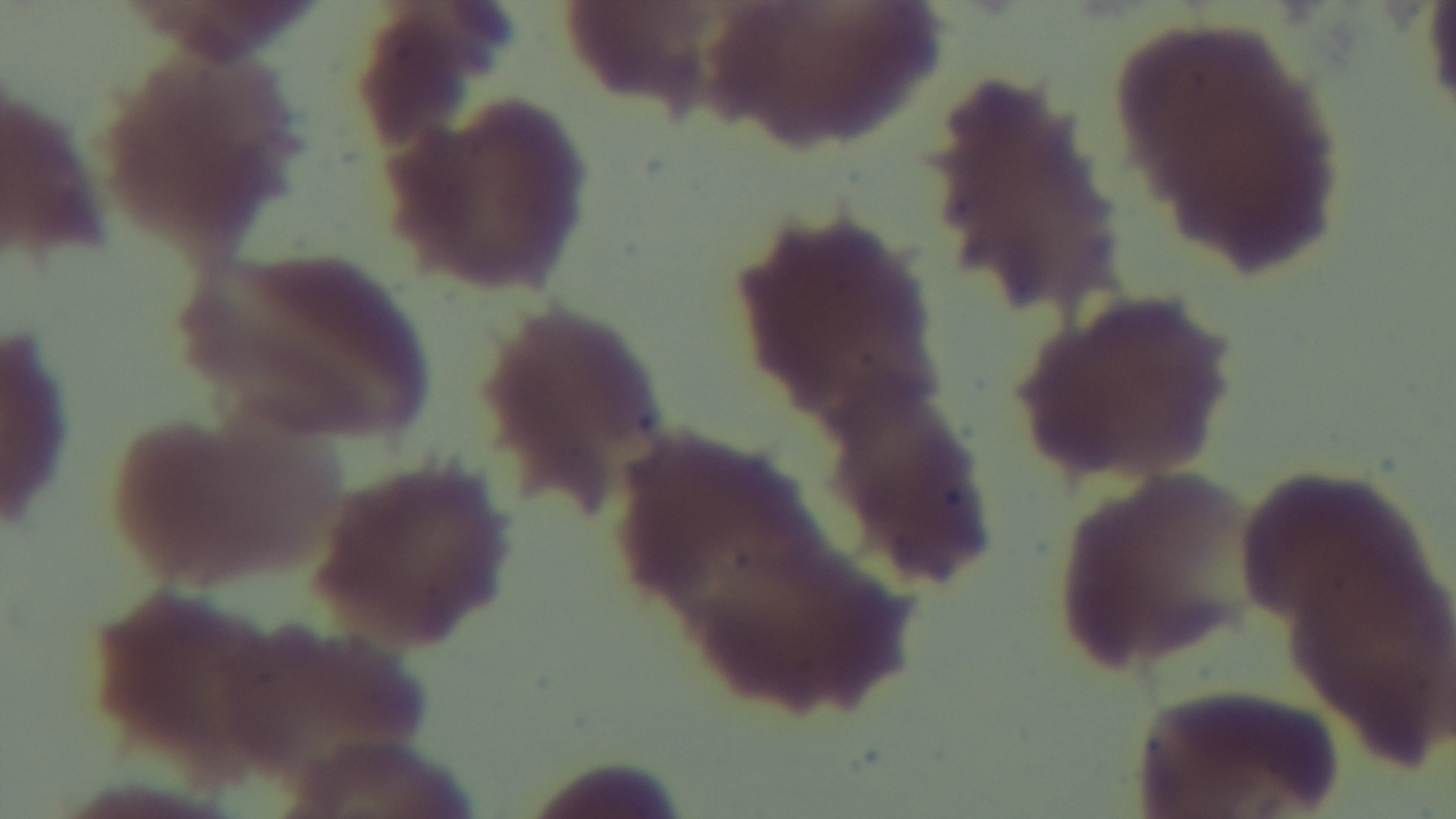 Malaria status: negative. Preparation: thin. Captured with a mounted 4K digital camera. Giemsa stain. Single field of view. Oil-immersion objective, 100x. Light microscopy.